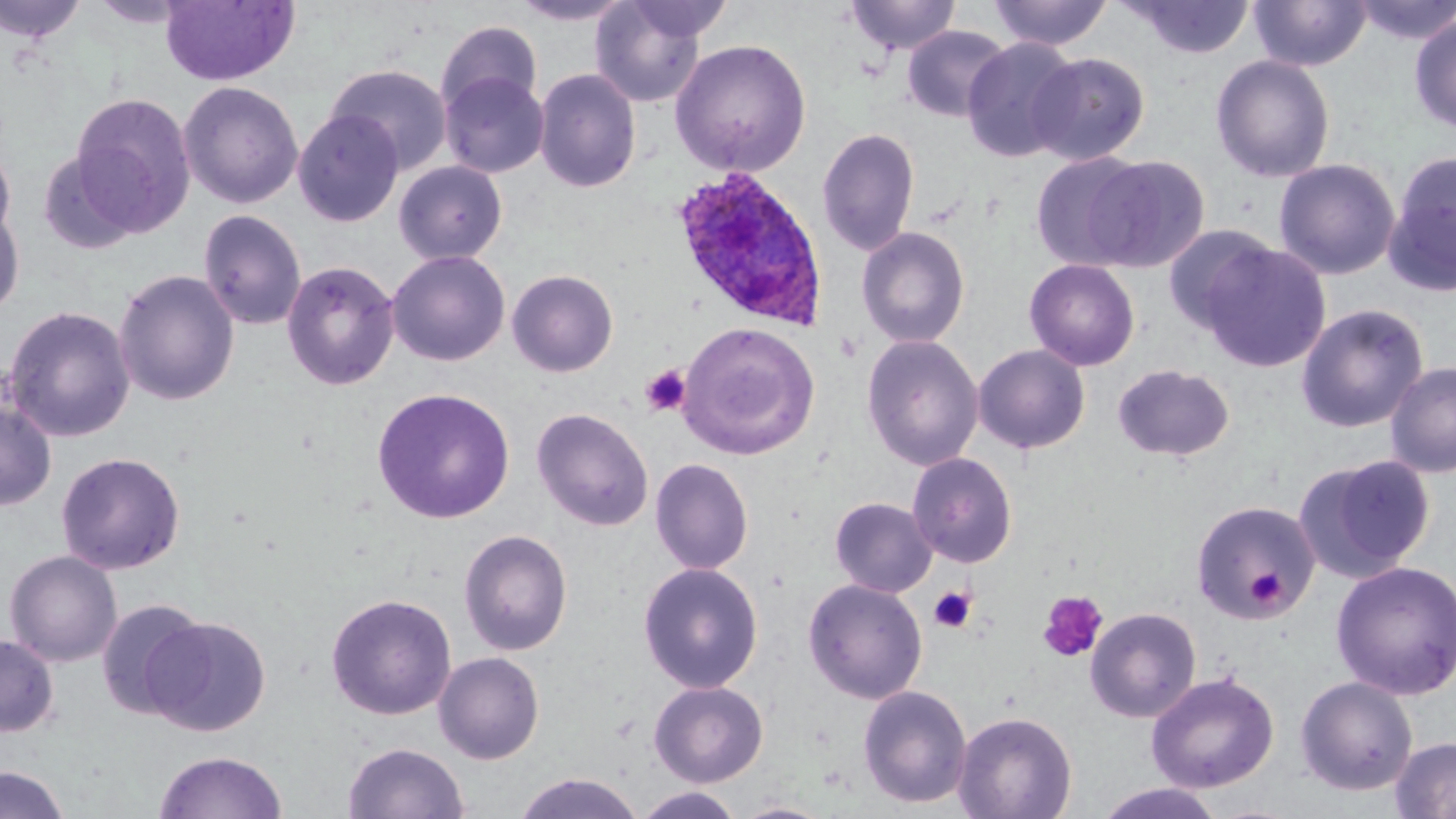
{
  "slide_level_diagnosis": "Plasmodium ovale",
  "stain": "May-Grünwald-Giemsa",
  "magnification": "1000x",
  "platelet_locations": "approximate bounding boxes as (x1, y1, x2, y2) in pixels: (639, 364, 691, 417), (1244, 565, 1288, 610), (928, 586, 977, 634), (1037, 589, 1109, 663)",
  "image_size": "1456×819 pixels",
  "plasmodium_ovale_infected_red_blood_cell_locations": "approximate bounding boxes as (x1, y1, x2, y2) in pixels: (669, 167, 827, 329)",
  "uninfected_red_blood_cell_locations": "approximate bounding boxes as (x1, y1, x2, y2) in pixels: (0, 0, 88, 43), (160, 0, 299, 86), (590, 0, 713, 108), (623, 0, 734, 42), (844, 0, 961, 56), (988, 0, 1113, 51), (1122, 0, 1256, 59), (1249, 0, 1372, 71), (1352, 0, 1456, 45), (89, 1, 193, 29), (509, 1, 633, 26), (1409, 13, 1456, 135), (436, 19, 543, 115), (901, 25, 1012, 122), (670, 38, 812, 177), (961, 38, 1082, 162), (1027, 52, 1150, 165), (1210, 54, 1336, 183), (326, 64, 453, 175), (533, 68, 642, 192), (441, 72, 549, 178), (178, 81, 304, 210), (69, 93, 196, 238), (293, 110, 404, 227), (817, 127, 920, 256), (0, 143, 16, 247), (37, 149, 141, 254), (1383, 150, 1456, 297), (1030, 152, 1151, 271), (1082, 155, 1211, 271), (1273, 158, 1400, 280), (394, 160, 508, 265), (0, 206, 24, 320), (197, 209, 307, 331), (1162, 224, 1278, 334), (856, 226, 970, 348), (1200, 241, 1331, 372), (387, 250, 510, 366), (1024, 259, 1140, 371), (282, 260, 400, 391), (113, 269, 240, 407), (507, 269, 618, 377), (1295, 302, 1429, 433), (2, 305, 136, 442), (678, 321, 820, 459), (861, 334, 984, 471), (973, 344, 1090, 455), (1384, 361, 1456, 478), (1112, 363, 1236, 462), (371, 387, 515, 524), (0, 398, 57, 511), (532, 407, 653, 531), (55, 451, 186, 575), (907, 452, 1017, 568), (1297, 454, 1436, 582), (650, 458, 754, 574), (829, 497, 937, 597), (1190, 499, 1321, 621), (458, 529, 573, 656), (4, 550, 122, 667), (1331, 560, 1456, 700), (638, 561, 764, 693), (803, 578, 928, 704), (326, 592, 457, 720), (95, 598, 209, 720), (1085, 606, 1202, 723), (144, 615, 270, 737), (0, 634, 59, 737), (433, 652, 544, 764), (1146, 672, 1279, 793), (1295, 675, 1418, 795), (649, 680, 769, 787), (857, 684, 973, 808), (953, 711, 1077, 819), (1390, 736, 1456, 819), (342, 741, 469, 819), (153, 750, 288, 819), (0, 765, 69, 819), (512, 772, 645, 819), (1093, 783, 1228, 819), (632, 787, 746, 819), (732, 801, 837, 819)",
  "preparation": "thin blood film",
  "modality": "light microscopy",
  "field_of_view": "single"
}